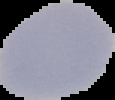

The area outside the segmented cell region is set to black. From a thin blood film. Image is 115×100 pixels. Result: negative for Plasmodium parasites.